Classify this cell by malaria status.
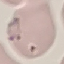
Parasitized.

Summary:
  - Capture: smartphone camera at the microscope eyepiece
  - Stain: Giemsa
  - Image type: cell patch, automatically extracted from a larger field of view and resized to 64 × 64 pixels
  - Preparation: thin smear